Name the parasite shown.
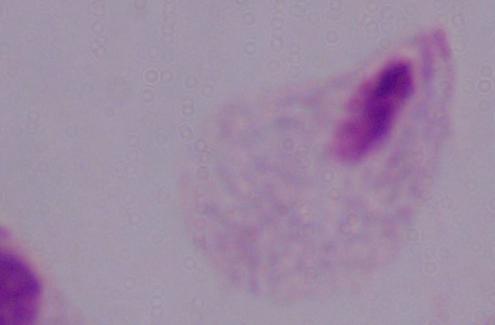
This is a trichomonad.

Micrograph. Captured at 1000x magnification.